Mark where platelets are.
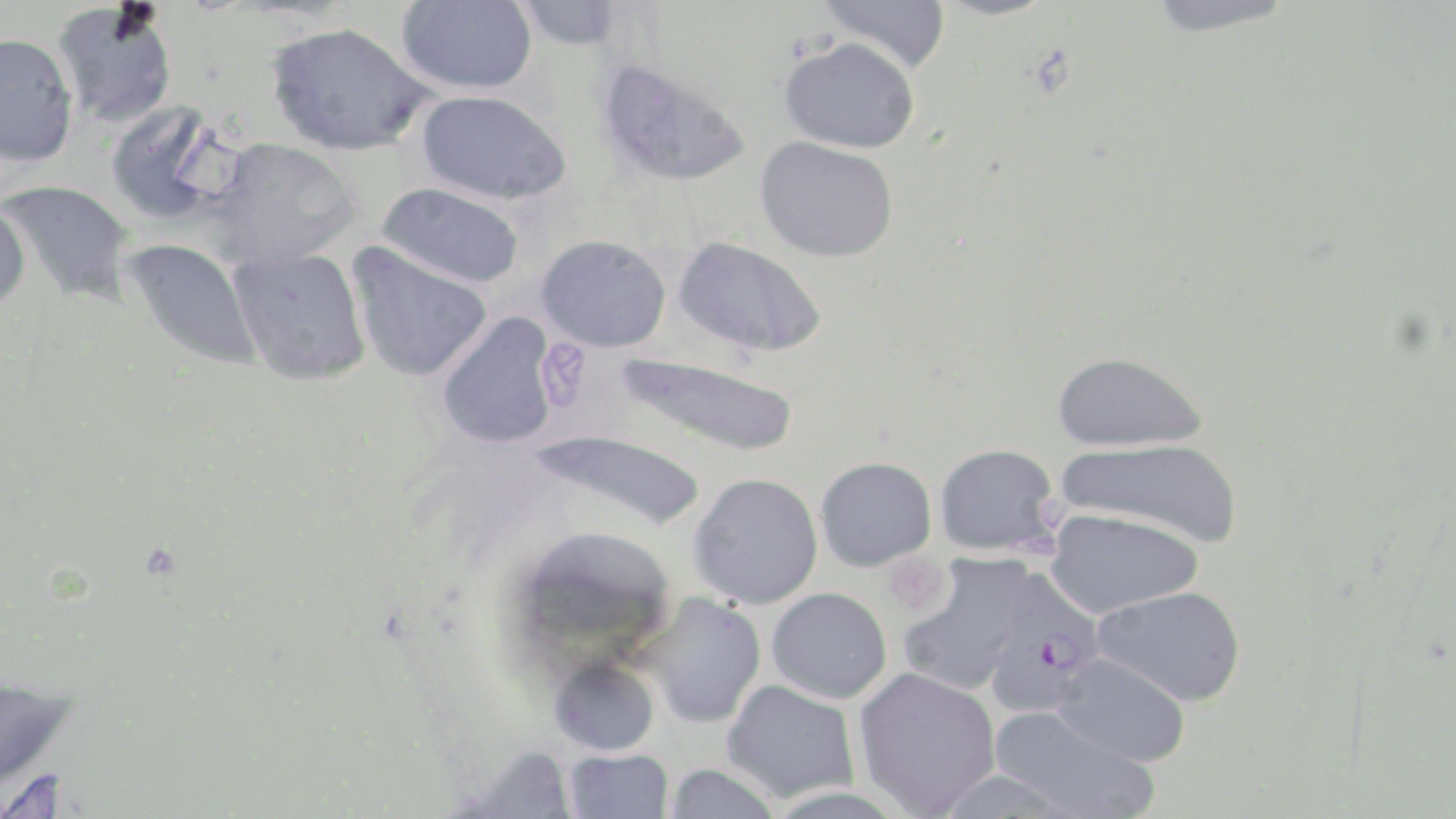

Approximate bounding boxes as (x1, y1, x2, y2) in pixels.
Platelets: (542, 337, 590, 412), (883, 554, 950, 616).

Plasmodium falciparum-infected red blood cell locations: (983, 568, 1106, 713). Uninfected red blood cell locations: (397, 0, 538, 94), (819, 0, 952, 73), (1144, 0, 1302, 36), (514, 1, 624, 51), (52, 2, 178, 130), (266, 22, 434, 156), (0, 31, 79, 168), (779, 36, 921, 153), (596, 58, 752, 188), (417, 90, 571, 206), (105, 102, 235, 227), (756, 136, 899, 262), (204, 137, 362, 269), (1, 179, 135, 307), (377, 183, 525, 289), (0, 197, 30, 317), (537, 234, 671, 352), (673, 235, 827, 358), (121, 238, 263, 374), (347, 243, 493, 383), (228, 247, 371, 386), (435, 312, 561, 450), (615, 351, 801, 457), (1053, 351, 1207, 452), (525, 428, 706, 531), (1058, 438, 1244, 548), (935, 443, 1061, 555), (815, 456, 936, 571), (689, 472, 823, 609), (1046, 509, 1202, 618), (899, 557, 1034, 695), (1093, 585, 1247, 706), (767, 588, 892, 703), (638, 592, 767, 728), (1052, 653, 1191, 767), (549, 657, 660, 756), (853, 667, 1001, 817), (0, 677, 79, 800), (722, 679, 861, 802), (989, 705, 1161, 819), (452, 744, 579, 818), (563, 748, 675, 819), (663, 764, 783, 818). Slide-level diagnosis: Plasmodium falciparum. Single field of view. Thin blood smear. Captured at 1000x magnification. Image is 1456×819 pixels. Optical microscopy. May-Grünwald-Giemsa stain.